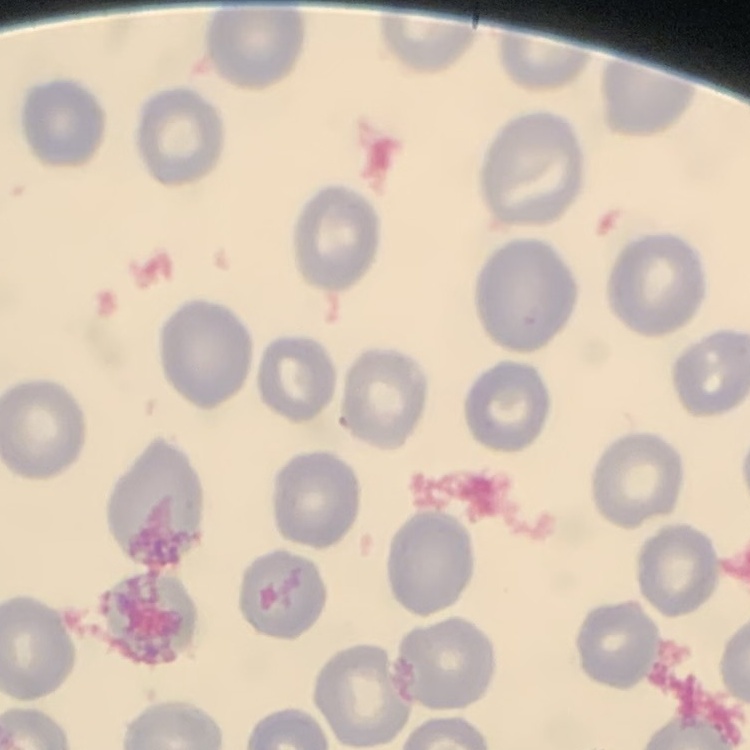 The erythrocytes show no rouleaux formation. Thin blood smear. Square crop of a larger photomicrograph. Field's or Giemsa stain.